Locate and identify every blood parasite.
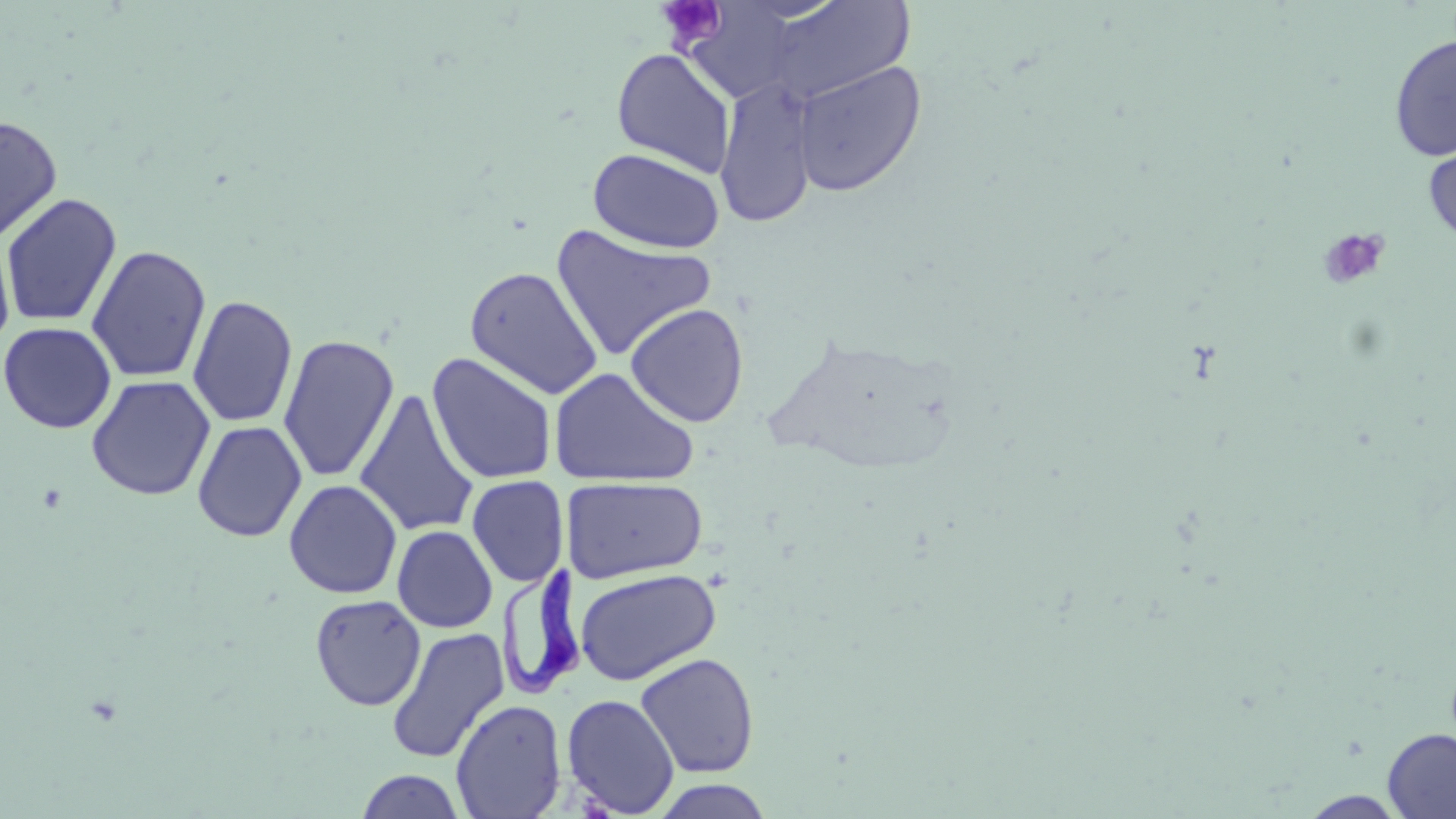
Approximate bounding boxes as [x1, y1, x2, y2] in pixels.
Trypanosoma brucei: [499, 568, 584, 698].
No Plasmodium falciparum, Plasmodium ovale, Plasmodium malariae, Plasmodium vivax, or Babesia divergens observed.

Platelet locations: [657, 1, 728, 50], [1317, 226, 1390, 291]. Uninfected red blood cell locations: [759, 0, 916, 105], [1388, 34, 1456, 162], [611, 48, 735, 177], [792, 60, 926, 197], [713, 76, 818, 229], [0, 114, 63, 244], [1422, 134, 1456, 250], [587, 147, 725, 254], [1, 193, 122, 328], [550, 224, 717, 361], [0, 233, 15, 352], [85, 244, 212, 383], [464, 265, 604, 400], [187, 294, 298, 428], [625, 302, 749, 428], [1, 321, 117, 434], [278, 334, 399, 484], [426, 352, 558, 486], [549, 366, 698, 487], [86, 375, 216, 501], [354, 388, 480, 537], [192, 420, 307, 542], [467, 474, 568, 587], [563, 475, 708, 584], [283, 478, 403, 599], [392, 524, 498, 633], [574, 567, 722, 686], [309, 593, 426, 711], [386, 627, 509, 764], [635, 652, 760, 778], [561, 693, 678, 816], [450, 698, 567, 819], [1382, 728, 1456, 819], [354, 769, 466, 818], [647, 778, 778, 819]. Slide-level diagnosis: Trypanosoma brucei. 1000x magnification. Image is 1456×819 pixels. May-Grünwald-Giemsa stain. Single field of view. Thin blood film. Light microscopy.